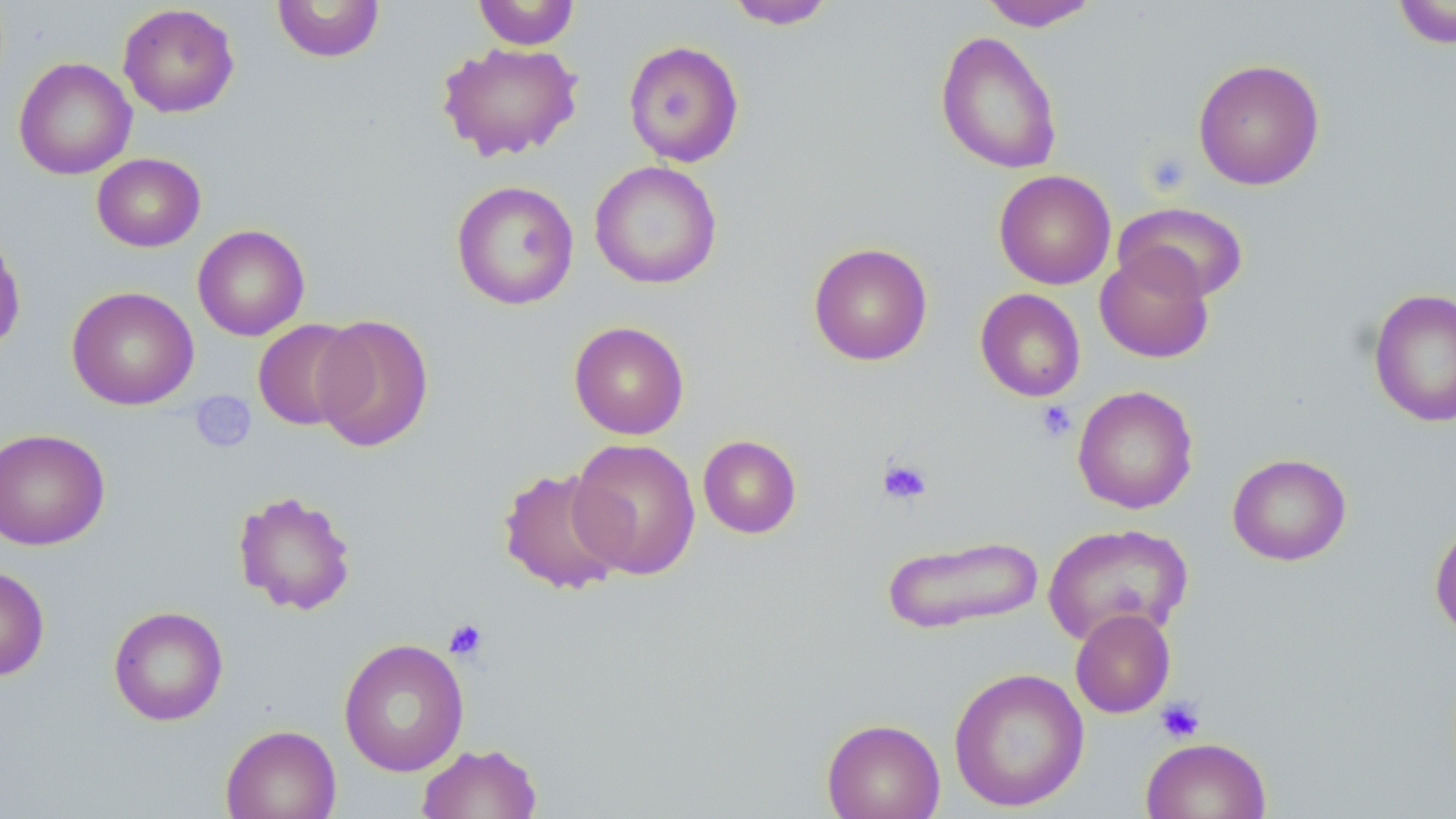
slide-level diagnosis = negative for blood parasites
modality = light microscopy
stain = May-Grünwald-Giemsa
magnification = 1000x
platelet locations = approximate bounding boxes as (x1, y1, x2, y2) in pixels: (1142, 149, 1194, 196), (190, 392, 257, 453), (1035, 400, 1077, 442), (876, 457, 932, 505), (443, 618, 489, 661), (1155, 697, 1205, 743)
image size = 1456×819 pixels
field of view = one of a larger specimen
uninfected red blood cell locations = approximate bounding boxes as (x1, y1, x2, y2) in pixels: (472, 0, 581, 50), (978, 0, 1100, 31), (271, 1, 386, 63), (724, 1, 839, 29), (1391, 1, 1456, 48), (117, 3, 239, 118), (935, 30, 1063, 175), (623, 40, 745, 168), (437, 42, 583, 162), (13, 57, 137, 180), (1192, 58, 1325, 190), (91, 152, 206, 252), (590, 160, 722, 290), (994, 170, 1116, 289), (451, 179, 580, 310), (1114, 201, 1249, 303), (192, 224, 310, 341), (0, 231, 26, 354), (808, 242, 932, 365), (1095, 248, 1214, 363), (66, 286, 199, 410), (1368, 287, 1456, 429), (974, 288, 1086, 402), (312, 314, 434, 453), (252, 319, 364, 431), (568, 320, 690, 440), (1073, 385, 1199, 514), (0, 428, 111, 551), (698, 434, 802, 539), (568, 436, 702, 580), (1227, 453, 1351, 566), (498, 467, 632, 596), (233, 489, 358, 616), (1429, 516, 1456, 640), (1043, 522, 1193, 646), (881, 534, 1043, 635), (0, 566, 50, 680), (108, 606, 229, 726), (1070, 608, 1176, 718), (338, 638, 470, 776), (948, 667, 1089, 812), (821, 717, 945, 819), (220, 724, 341, 819), (1140, 736, 1271, 819), (416, 743, 543, 819)
preparation = thin blood film